Point out each Plasmodium parasite.
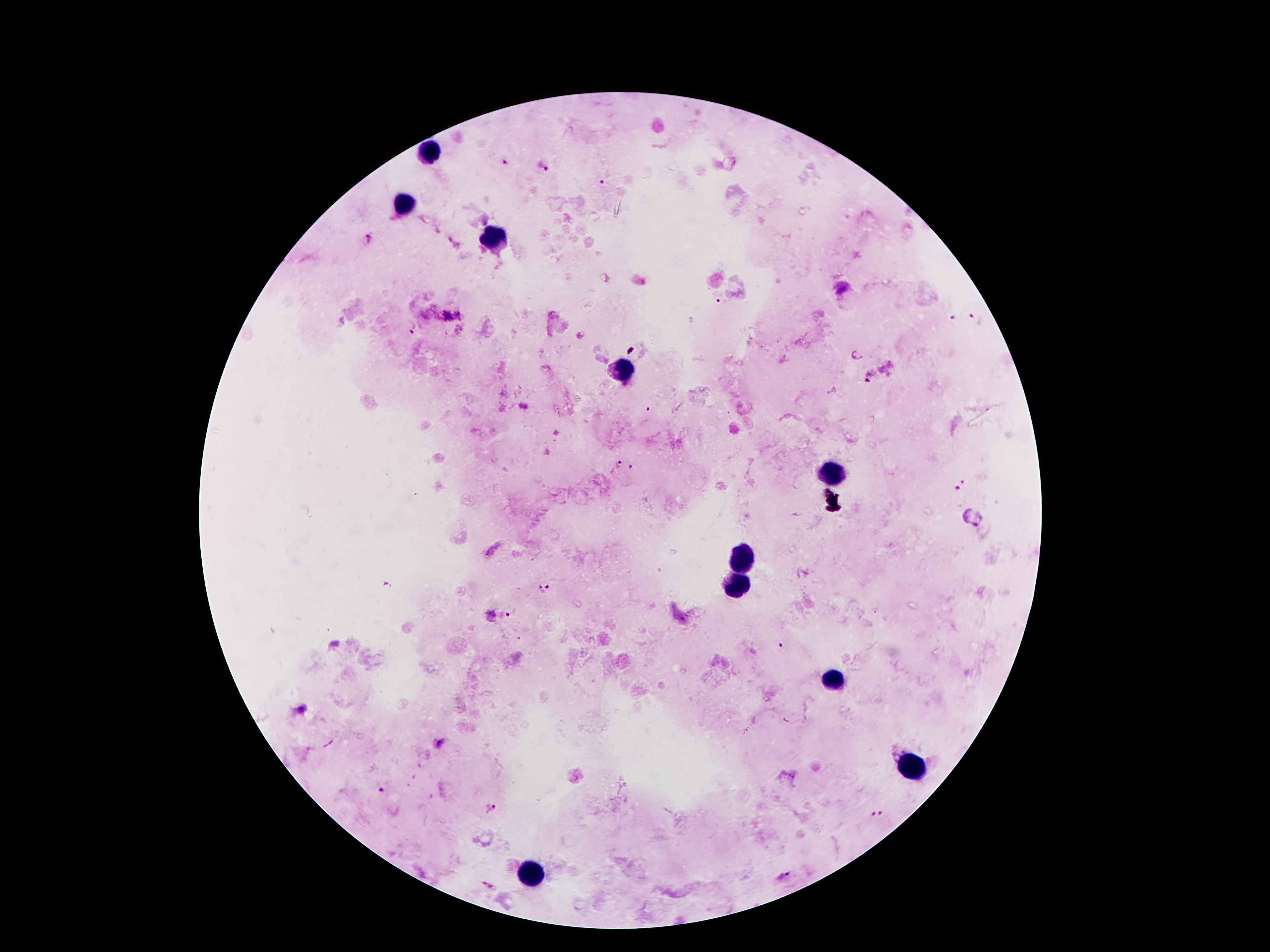

Approximate centers as {x, y} in pixels.
Plasmodium parasites: {505, 161}, {543, 166}, {603, 182}, {719, 303}, {974, 318}, {952, 320}, {412, 327}, {648, 410}, {619, 464}, {633, 468}, {965, 481}, {955, 489}, {546, 589}, {507, 614}, {782, 649}, {382, 790}, {490, 808}, {881, 813}, {870, 815}, {787, 875}.

field_of_view: single
leukocyte_locations: 'approximate centers as {x, y} in pixels: {430, 154}, {407, 205}, {494, 241}, {621, 368}, {832, 474}, {743, 562}, {734, 587}, {834, 685}, {907, 766}, {532, 876}'
magnification: 100x
stain: Giemsa
preparation: thick peripheral-blood smear
capture: smartphone camera through the microscope eyepiece
image_size: 1270×952 pixels
patient_malaria_status: infected with Plasmodium falciparum